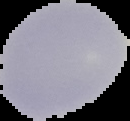

Summary:
  - Preparation: thin blood film
  - Result: no malaria parasites detected
  - Image size: 130×121 pixels
  - Image type: segmented cell region with the area outside set to black